Point out Plasmodium parasites and leukocytes.
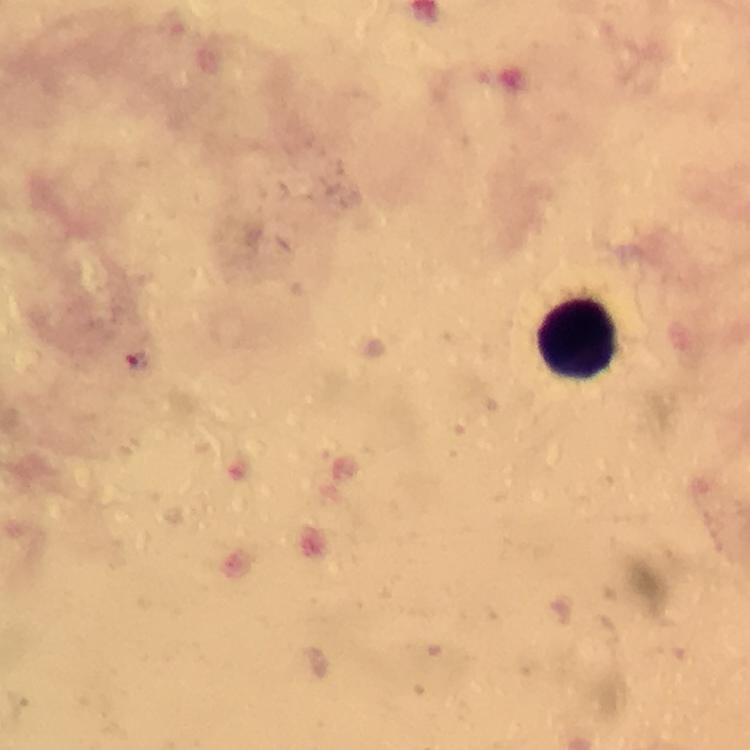
Approximate centers as (x, y) in pixels.
Plasmodium parasites: (138, 360).
Leukocytes: (578, 337).

image_size: 750×750 pixels
stain: Giemsa
preparation: thick blood smear
immersion_oil: used
context: from a malaria diagnostic workup
capture: smartphone photograph through a microscope
magnification: 100x
cropped_from: one field of view